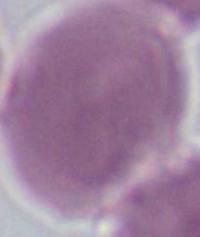
1000x magnification. Photomicrograph. An erythrocyte is seen.